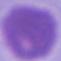
modality = micrograph
magnification = 1000x
identification = red blood cell